Describe the morphology of the erythrocytes.
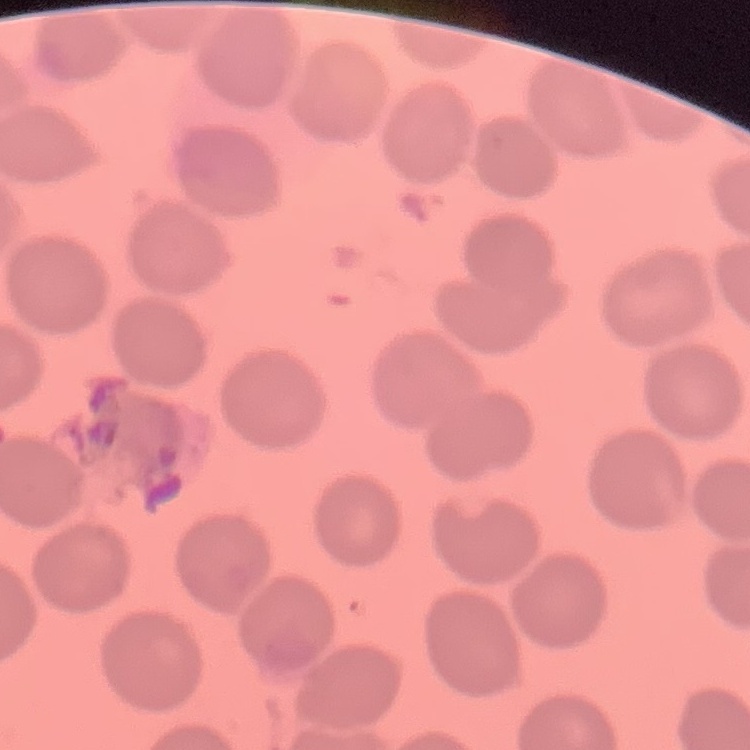
No rouleaux formation.

Thin blood smear. Stained with either Field's or Giemsa. Square crop of a larger photomicrograph.